Locate and identify every blood parasite.
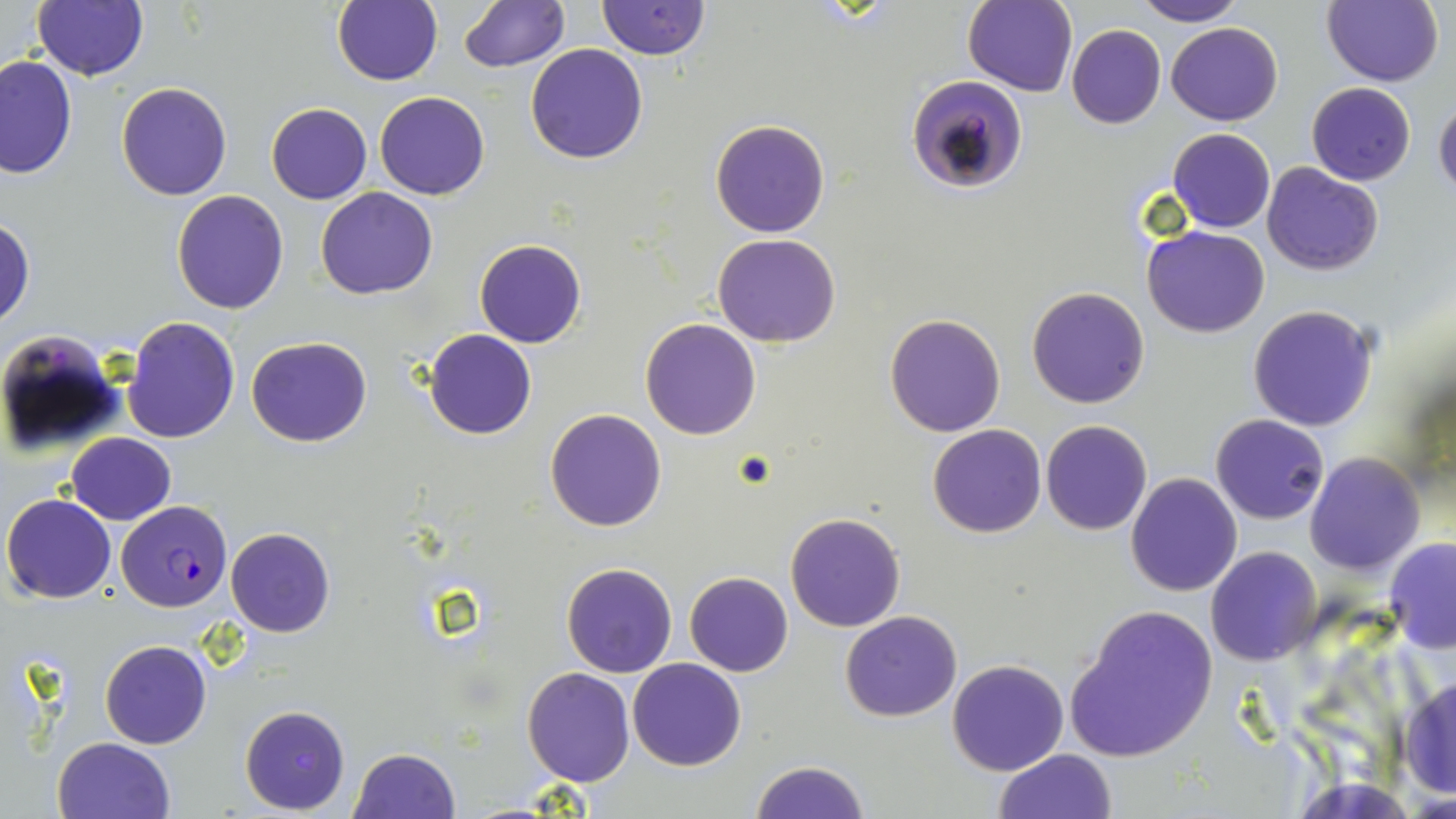

Approximate bounding boxes as (x1,y1)-(x2,y2) corner pairs in pixels.
Plasmodium falciparum-infected red blood cells: (908,75)-(1029,195), (117,505)-(233,612).
No Plasmodium ovale, Plasmodium malariae, Plasmodium vivax, Babesia divergens, or Trypanosoma brucei observed.

Uninfected red blood cell locations: (332,0)-(442,85), (598,0)-(709,59), (964,0)-(1076,95), (1321,0)-(1443,87), (32,1)-(149,81), (459,1)-(569,72), (1131,1)-(1245,26), (968,14)-(1165,120), (1165,23)-(1283,125), (1065,25)-(1166,129), (525,44)-(648,165), (0,54)-(77,180), (117,82)-(233,201), (1306,82)-(1416,185), (375,91)-(489,200), (1433,96)-(1456,200), (266,102)-(371,204), (710,119)-(830,238), (1168,127)-(1275,232), (1261,162)-(1383,275), (315,187)-(438,299), (171,190)-(290,313), (0,219)-(33,329), (1143,226)-(1270,338), (714,233)-(840,348), (474,239)-(587,348), (1026,287)-(1150,409), (1248,305)-(1379,431), (885,312)-(1006,437), (122,315)-(238,443), (641,319)-(762,440), (0,326)-(128,460), (423,329)-(536,439), (247,336)-(371,448), (544,407)-(668,531), (1211,413)-(1328,525), (1042,420)-(1151,535), (928,424)-(1046,538), (66,432)-(176,523), (1304,453)-(1425,575), (1125,472)-(1243,597), (1,493)-(117,604), (785,512)-(906,631), (225,527)-(335,637), (1383,539)-(1456,655), (1206,547)-(1323,665), (561,563)-(677,678), (684,572)-(794,676), (1064,604)-(1217,763), (842,611)-(962,721), (100,639)-(212,749), (627,658)-(747,771), (947,659)-(1068,776), (521,667)-(635,787), (1399,673)-(1456,800), (239,705)-(350,814), (53,737)-(177,819), (348,747)-(461,819), (994,749)-(1116,819), (749,759)-(871,819). Slide-level diagnosis: Plasmodium falciparum. Single field of view. May-Grünwald-Giemsa stain. Image is 1456×819 pixels. Captured at 1000x magnification. Light microscopy. Thin blood smear.